Identify the cell.
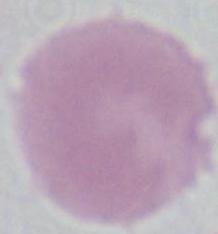

This is an erythrocyte.

modality = micrograph
magnification = 1000x